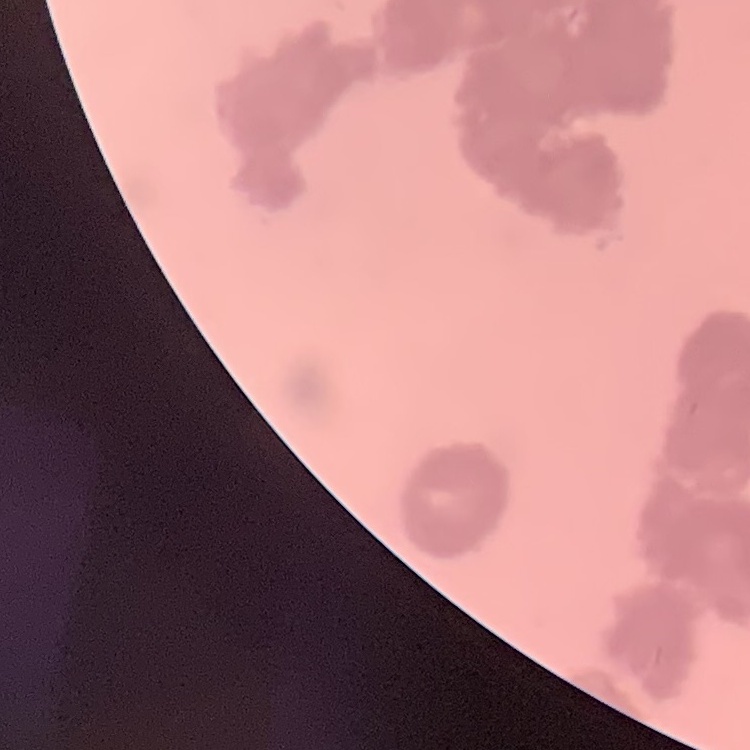
The red blood cells show rouleaux formation. One tile cut from a larger photomicrograph. Thin blood film. Field's or Giemsa stain.